Assess the morphology of the red blood cells.
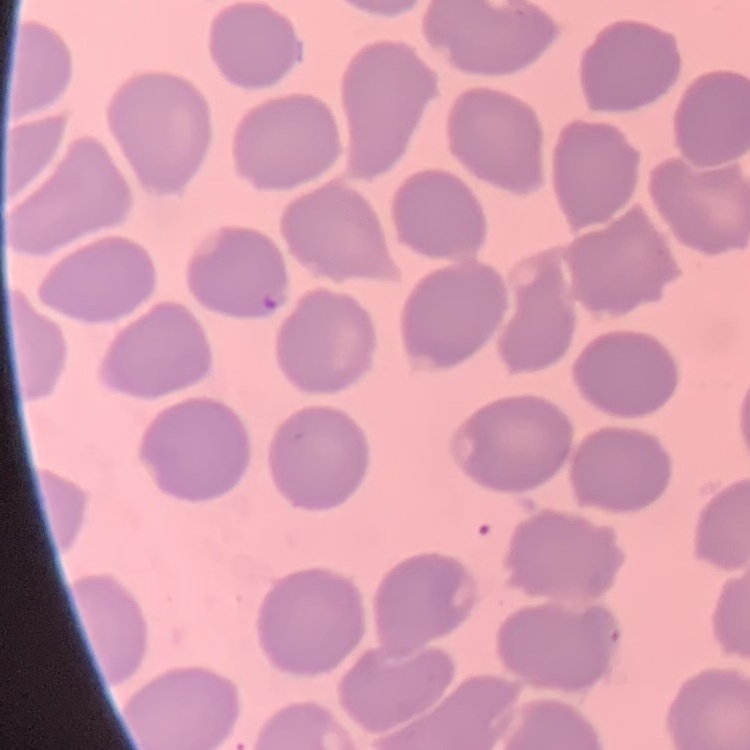
No rouleaux formation.

Thin blood film. Stained with either Field's or Giemsa. Square crop of a larger photomicrograph.